Classify this cell by malaria status.
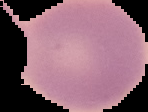

Uninfected.

Summary:
  - Image size: 148×112 pixels
  - Image type: cell region segmented out of the field of view; surrounding area masked to black
  - Preparation: thin blood film